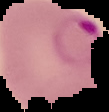
image size = 109×112 pixels
preparation = thin blood film
malaria status = parasitized
image type = segmented cell region on a black background